Classify this cell by malaria status.
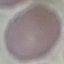
It is uninfected.

Thin smear of blood. Photographed with a smartphone camera at the microscope eyepiece. Giemsa stain. Automatically extracted cell patch, resized to 64 × 64 pixels.